Locate every leukocyte (white blood cell).
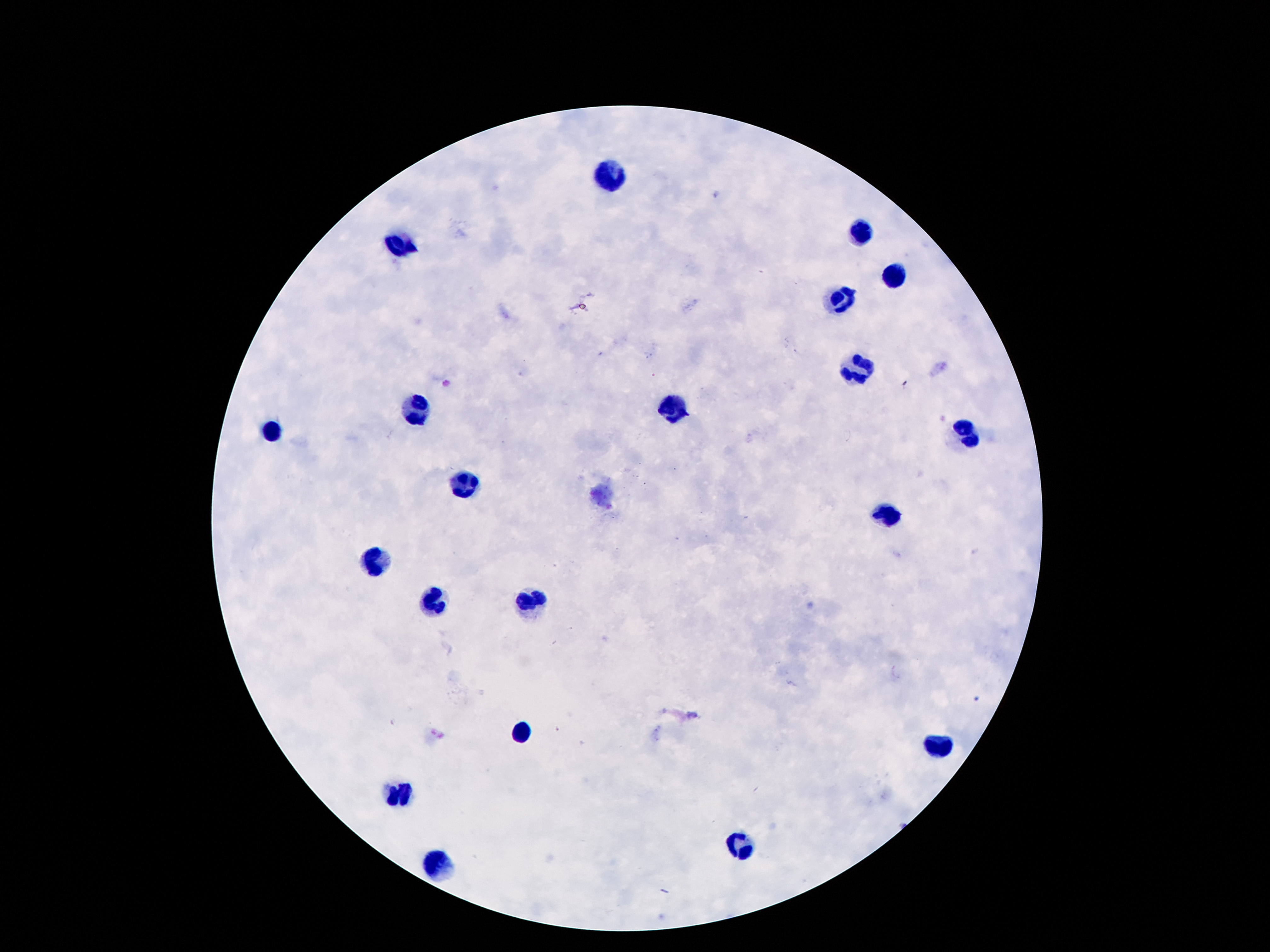

Approximate centers as {x, y} in pixels.
Leukocytes: {614, 174}, {864, 235}, {400, 248}, {891, 276}, {843, 300}, {864, 372}, {417, 409}, {671, 409}, {272, 430}, {971, 430}, {469, 482}, {885, 516}, {379, 562}, {534, 602}, {435, 604}, {522, 733}, {937, 748}, {396, 792}, {740, 845}, {438, 864}.

Summary:
  - Capture: smartphone camera through the microscope eyepiece
  - Field of view: single
  - Patient malaria status: uninfected
  - Preparation: thick peripheral-blood smear
  - Stain: Giemsa
  - Magnification: 100x
  - Image size: 1270×952 pixels